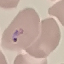
Summary:
  - Malaria status: parasitized
  - Preparation: thin blood smear
  - Image type: cell patch, automatically extracted from a larger field of view and resized to 64 × 64 pixels
  - Capture: smartphone camera at the microscope eyepiece
  - Stain: Giemsa